Comment on the morphology of the erythrocytes.
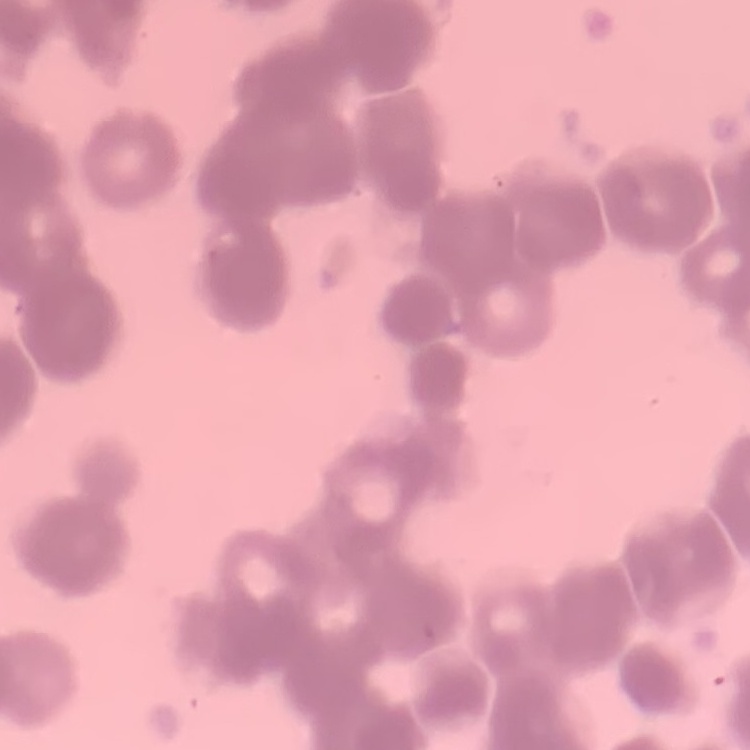

Rouleaux formation.

{
  "preparation": "thin peripheral smear",
  "image_type": "one tile cut from a larger photomicrograph",
  "stain": "Field's or Giemsa"
}